Outline each uninfected red blood cell.
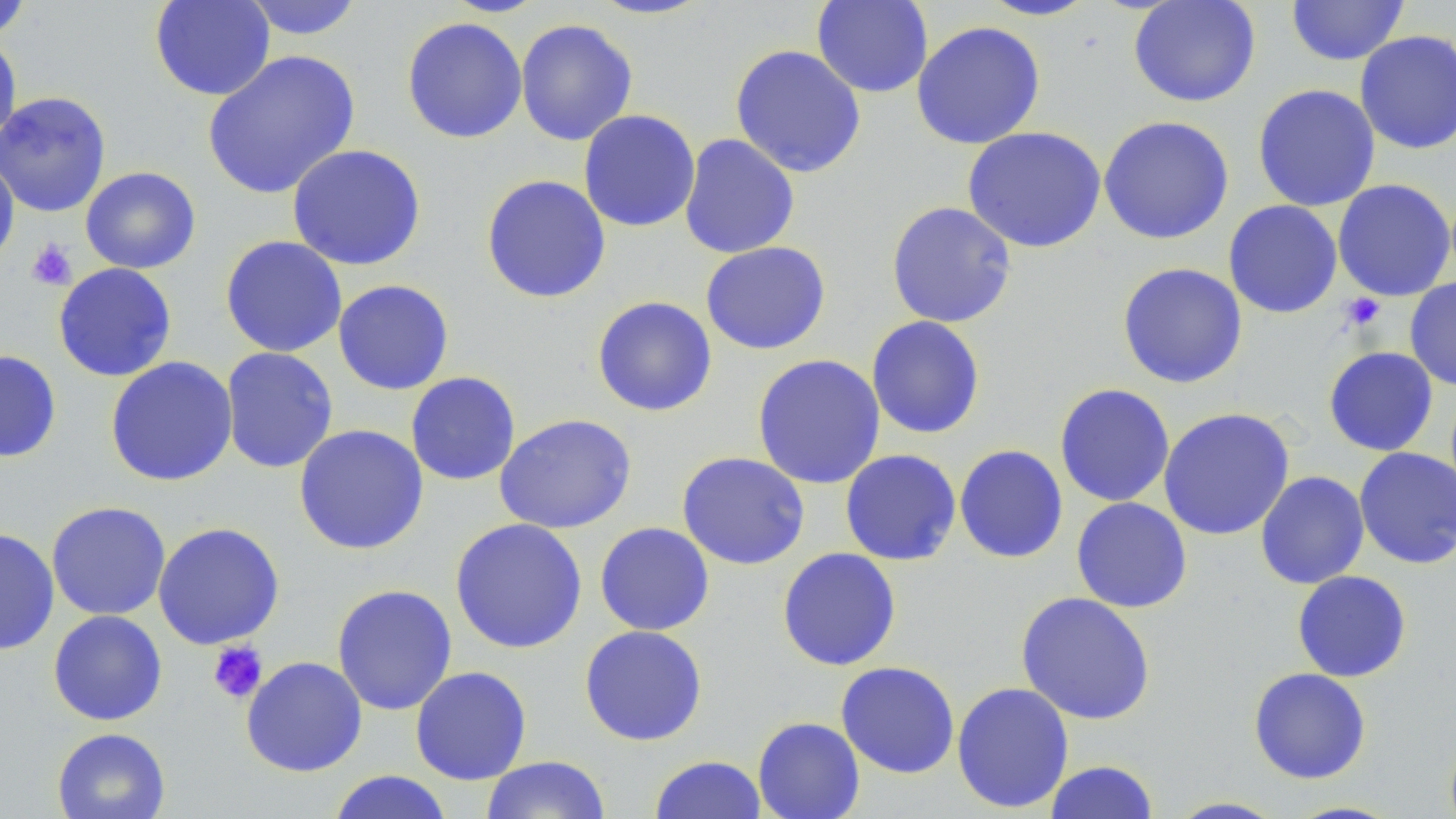

Approximate bounding boxes as (x1, y1, x2, y2) in pixels.
Uninfected red blood cells: (149, 0, 276, 101), (240, 0, 367, 41), (587, 0, 717, 21), (811, 0, 933, 98), (978, 0, 1101, 21), (1128, 0, 1261, 107), (1285, 0, 1410, 66), (0, 1, 36, 40), (401, 15, 528, 144), (515, 18, 638, 146), (911, 20, 1046, 149), (1355, 29, 1456, 155), (0, 31, 22, 149), (729, 44, 867, 178), (202, 49, 361, 200), (1252, 83, 1381, 212), (0, 91, 112, 218), (578, 109, 701, 233), (1098, 115, 1235, 245), (962, 126, 1107, 253), (679, 133, 800, 259), (286, 144, 427, 271), (0, 156, 20, 269), (80, 167, 201, 274), (480, 174, 611, 304), (1332, 178, 1456, 302), (1223, 200, 1343, 318), (886, 201, 1017, 329), (220, 235, 348, 358), (700, 241, 831, 355), (52, 262, 178, 382), (1116, 262, 1248, 389), (1405, 277, 1456, 391), (332, 279, 455, 395), (591, 296, 718, 417), (866, 315, 985, 439), (220, 346, 339, 474), (1323, 346, 1438, 456), (0, 349, 62, 463), (751, 354, 886, 490), (104, 356, 238, 487), (405, 371, 521, 486), (1054, 383, 1176, 507), (1157, 407, 1295, 541), (494, 413, 637, 534), (293, 424, 429, 555), (954, 444, 1068, 564), (1354, 447, 1455, 569), (840, 448, 961, 566), (676, 451, 810, 570), (1255, 471, 1370, 589), (1071, 496, 1193, 613), (46, 500, 171, 621), (449, 517, 588, 654), (152, 521, 285, 650), (594, 522, 715, 636), (0, 527, 59, 655), (777, 547, 902, 671), (1291, 569, 1412, 683), (331, 583, 458, 716), (1015, 591, 1156, 725), (48, 610, 168, 726), (579, 625, 708, 746), (241, 656, 367, 777), (835, 661, 960, 779), (410, 666, 532, 785), (1248, 667, 1372, 784), (951, 681, 1075, 814), (752, 716, 866, 819), (51, 727, 171, 819), (1444, 730, 1456, 819), (649, 754, 767, 818), (480, 755, 611, 818), (1043, 759, 1160, 819), (326, 770, 454, 819), (1165, 796, 1288, 818), (1283, 800, 1406, 818).

Platelet locations: (26, 239, 77, 290), (1339, 293, 1386, 331), (207, 641, 268, 704). Slide-level diagnosis: negative for blood parasites. May-Grünwald-Giemsa stain. Thin blood film. Captured at 1000x magnification. Image is 1456×819 pixels. Optical microscopy. One field of a larger specimen.